Classify this cell by malaria status.
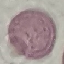
Uninfected.

Photographed with a smartphone camera at the microscope eyepiece. Giemsa-stained preparation. Thin blood film. Automatically extracted cell patch, resized to 64 × 64 pixels.